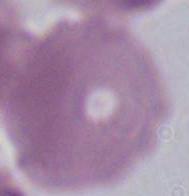
Summary:
  - Modality: photomicrograph
  - Magnification: 1000x
  - Identification: red blood cell